Identify the preparation type.
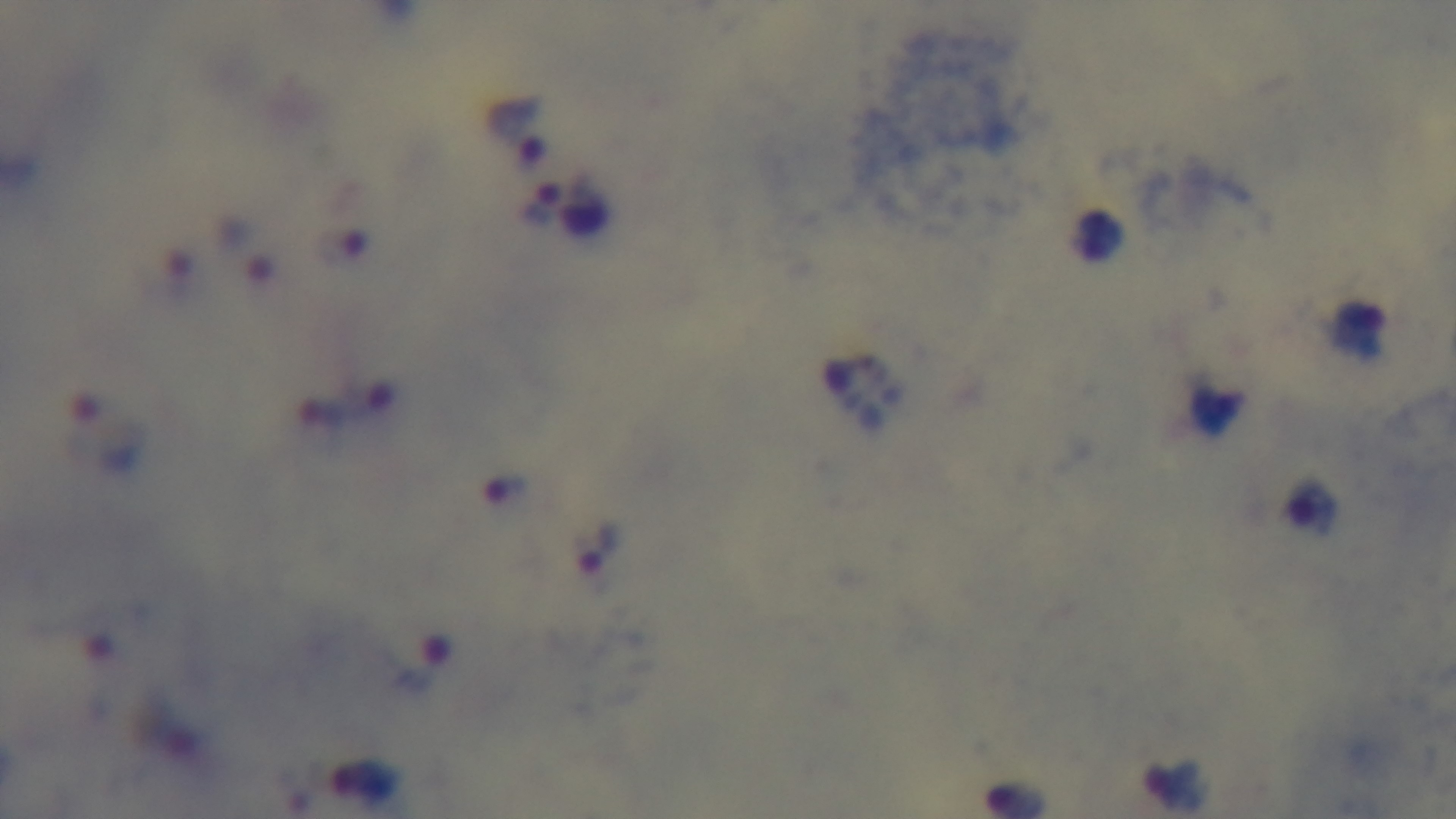
It is a thick blood film.

malaria status = positive
stain = Giemsa
objective = 100x oil immersion
capture = mounted 4K digital camera
field of view = one from the slide
modality = light microscopy